Locate every malaria parasite.
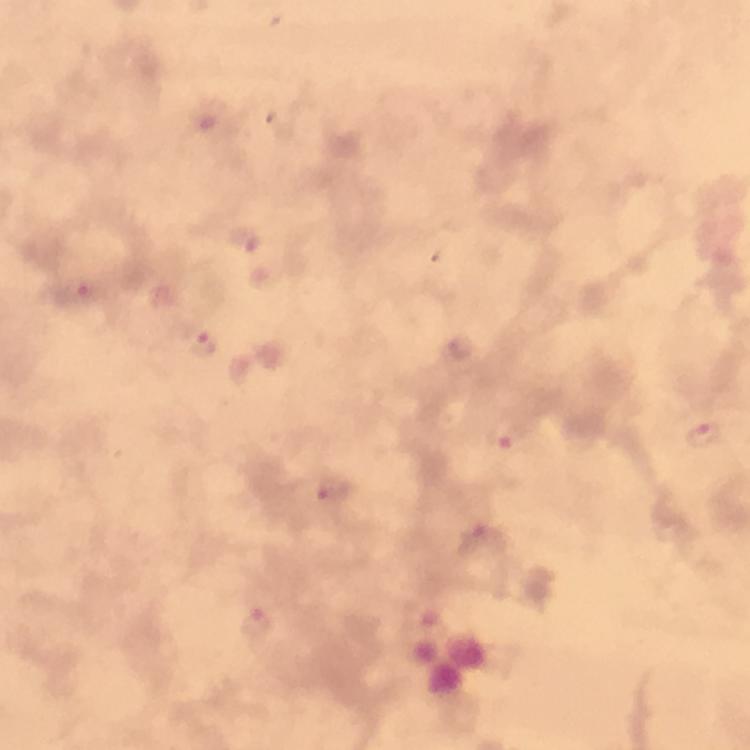
Approximate centers as {x, y} in pixels.
Malaria parasites: {243, 242}, {77, 292}, {203, 344}, {458, 351}, {703, 433}, {509, 436}, {331, 490}, {481, 539}, {257, 625}.

From a malaria diagnostic workup. 100x magnification. Photographed with a smartphone mounted on the microscope. Thick smear. Giemsa-stained preparation. Cropped region of a single field of view. Image is 750×750 pixels. Immersion oil applied.